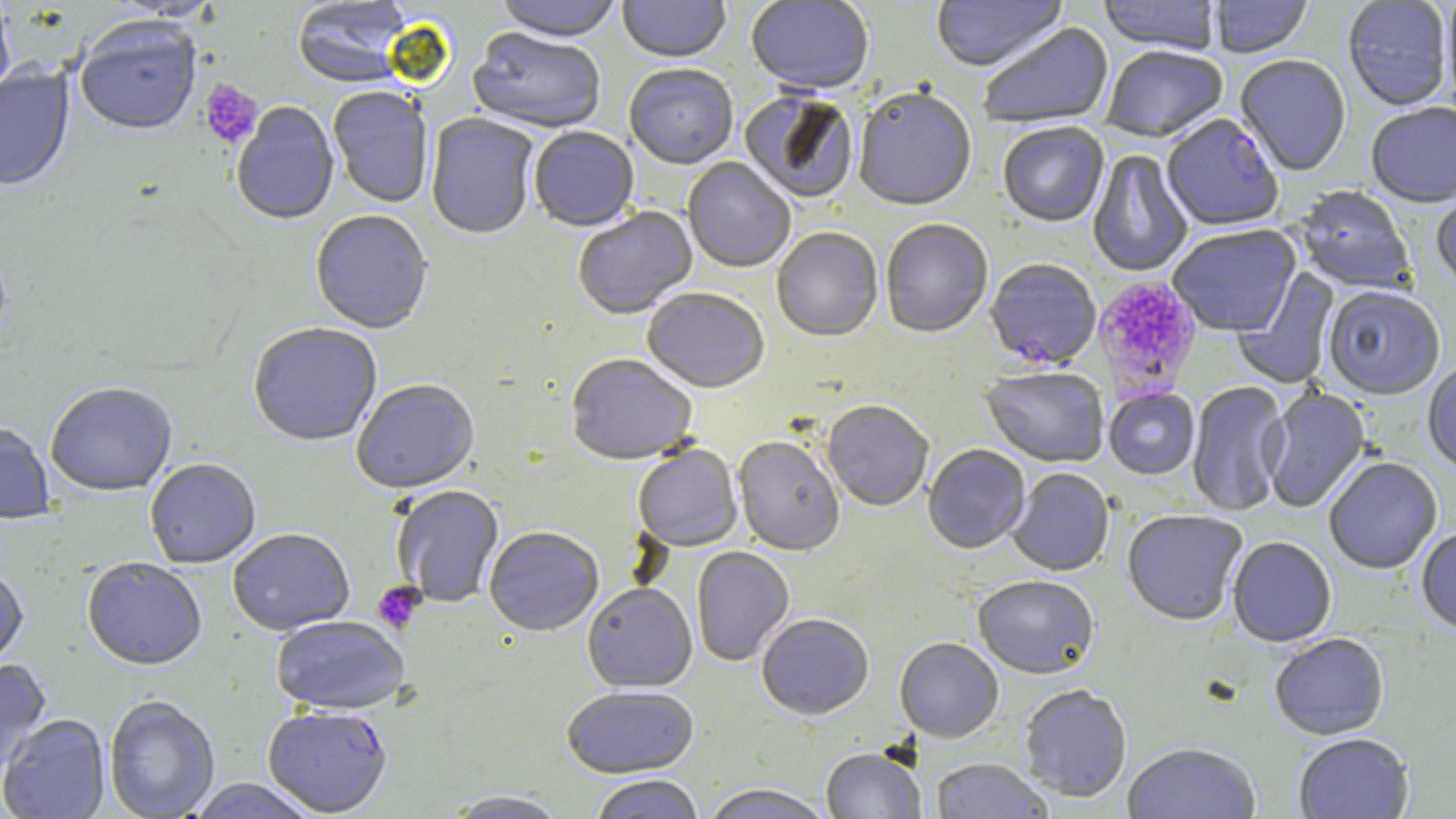
Approximate bounding boxes as [x1, y1, x2, y2] in pixels. Plasmodium falciparum-infected red blood cell locations: [1162, 115, 1283, 234], [984, 261, 1102, 372], [263, 706, 392, 817]. Uninfected red blood cell locations: [100, 0, 226, 22], [292, 0, 411, 90], [494, 0, 622, 45], [617, 0, 731, 65], [746, 0, 874, 96], [931, 0, 1068, 74], [1098, 0, 1220, 56], [1209, 0, 1313, 59], [1343, 1, 1452, 112], [1441, 1, 1456, 114], [0, 2, 15, 105], [76, 21, 201, 138], [979, 22, 1115, 131], [468, 29, 606, 136], [1102, 48, 1228, 145], [1235, 56, 1351, 177], [0, 64, 75, 193], [624, 66, 738, 171], [329, 88, 432, 208], [853, 90, 977, 213], [740, 93, 858, 206], [231, 102, 340, 227], [1366, 104, 1456, 209], [425, 113, 538, 242], [998, 124, 1109, 229], [529, 128, 639, 234], [1087, 150, 1193, 278], [682, 158, 796, 274], [1292, 187, 1415, 295], [1431, 190, 1456, 293], [574, 208, 698, 321], [310, 212, 433, 336], [880, 221, 993, 340], [1168, 226, 1301, 338], [771, 229, 883, 344], [1232, 267, 1340, 390], [1323, 288, 1445, 402], [642, 290, 769, 396], [247, 324, 382, 449], [566, 356, 696, 468], [1422, 364, 1456, 475], [981, 369, 1109, 469], [351, 381, 480, 495], [1186, 382, 1290, 517], [45, 384, 177, 498], [1261, 387, 1372, 514], [1104, 389, 1199, 481], [821, 402, 933, 513], [0, 423, 54, 525], [733, 438, 845, 557], [633, 445, 742, 552], [923, 445, 1031, 556], [1324, 458, 1443, 577], [145, 459, 261, 569], [1008, 469, 1114, 578], [391, 487, 504, 608], [1122, 511, 1247, 628], [484, 529, 603, 638], [1416, 529, 1456, 636], [228, 530, 354, 637], [1227, 538, 1337, 649], [692, 548, 795, 667], [82, 559, 207, 672], [0, 568, 28, 672], [973, 579, 1099, 681], [582, 585, 698, 694], [757, 616, 874, 723], [271, 618, 410, 716], [1270, 635, 1389, 741], [894, 639, 1004, 744], [0, 659, 52, 773], [1020, 686, 1132, 804], [561, 687, 700, 781], [104, 696, 219, 818], [0, 714, 110, 819], [1294, 735, 1414, 819], [1122, 745, 1261, 819], [821, 749, 924, 818], [930, 759, 1054, 819], [589, 777, 706, 819], [185, 779, 320, 819], [700, 786, 835, 819], [445, 792, 570, 819]. Platelet locations: [199, 80, 262, 150], [1092, 276, 1200, 401], [372, 582, 424, 635]. Slide-level diagnosis: Plasmodium falciparum. Thin blood film. May-Grünwald-Giemsa stain. Single field of view. Captured at 1000x magnification. Optical microscopy. Image is 1456×819 pixels.